Locate and identify every blood parasite.
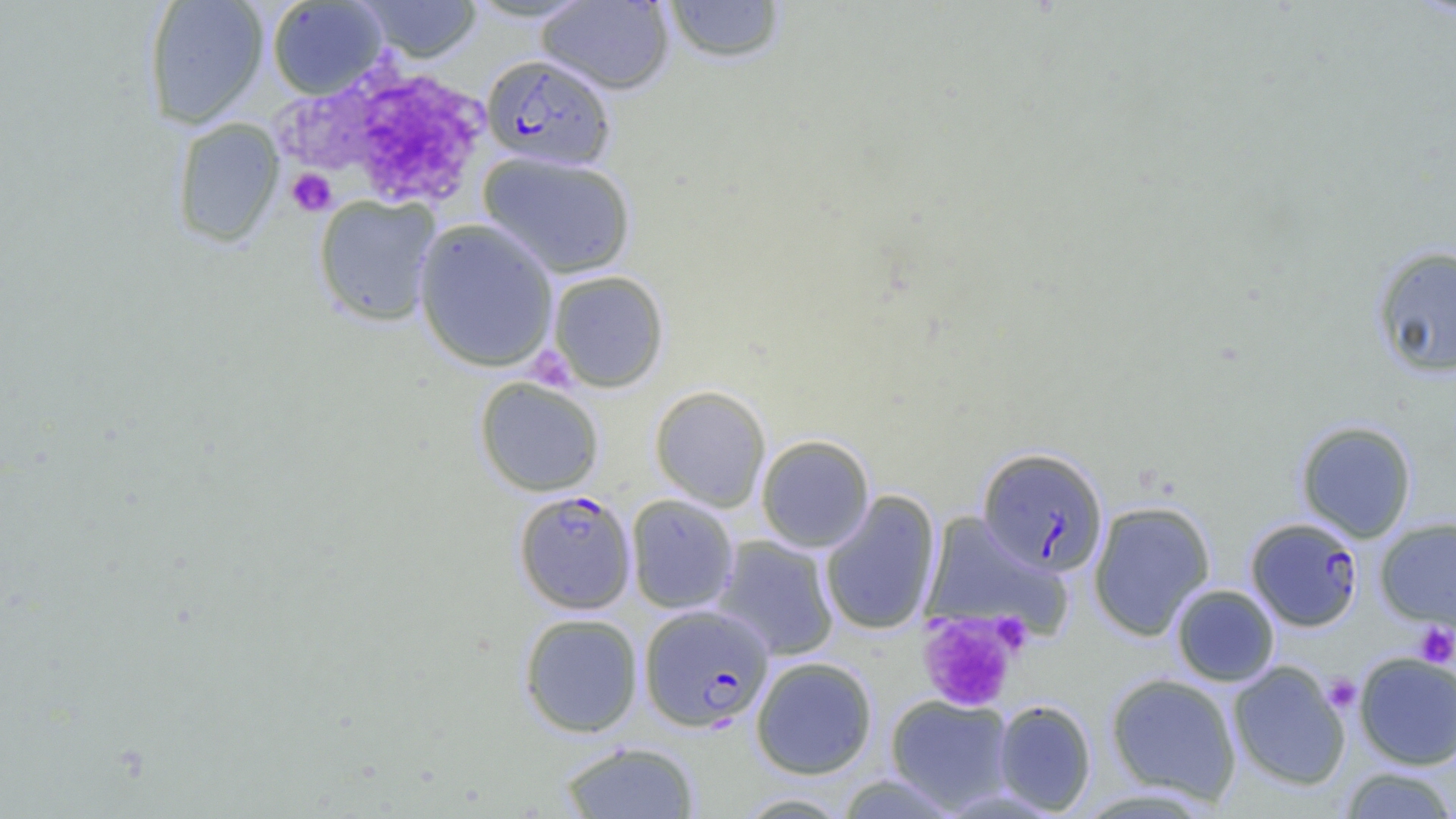

Approximate bounding boxes as (x1, y1, x2, y2) in pixels.
Plasmodium falciparum-infected red blood cells: (481, 54, 617, 171), (977, 447, 1109, 576), (514, 491, 636, 617), (1246, 517, 1363, 631), (639, 604, 774, 732).
No Plasmodium ovale, Plasmodium malariae, Plasmodium vivax, Babesia divergens, or Trypanosoma brucei observed.

Uninfected red blood cell locations: (143, 0, 269, 129), (461, 0, 599, 23), (267, 1, 388, 100), (356, 1, 482, 63), (536, 1, 674, 95), (661, 1, 788, 64), (171, 117, 284, 249), (478, 151, 637, 279), (313, 195, 442, 327), (413, 218, 559, 373), (1371, 245, 1456, 379), (546, 270, 670, 393), (474, 377, 605, 497), (649, 385, 771, 512), (1295, 420, 1417, 543), (756, 434, 875, 552), (820, 489, 941, 636), (626, 495, 739, 614), (1087, 500, 1215, 640), (920, 512, 1070, 640), (1375, 517, 1456, 631), (712, 535, 840, 660), (1171, 583, 1280, 686), (519, 612, 644, 738), (1354, 652, 1456, 770), (750, 656, 878, 779), (1227, 661, 1351, 791), (1105, 672, 1242, 804), (885, 694, 1015, 813), (993, 699, 1097, 815), (559, 740, 701, 819), (1338, 766, 1456, 818), (733, 792, 855, 818). Platelet locations: (294, 63, 487, 216), (286, 168, 337, 216), (527, 352, 568, 391), (918, 612, 1018, 713), (1414, 622, 1456, 668), (1323, 674, 1362, 713). Slide-level diagnosis: Plasmodium falciparum. Image is 1456×819 pixels. Thin blood film. One field of a larger specimen. Light microscopy. 1000x magnification.